Assess this cell for malaria.
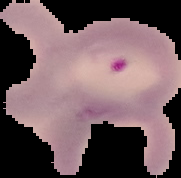
It is parasitized.

From a thin blood smear. Segmented cell region on a black background. Image is 181×178 pixels.